Name the parasite shown.
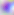
Toxoplasma gondii.

Photomicrograph. 400x magnification.